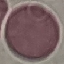
{
  "result": "negative for malaria parasites",
  "capture": "smartphone camera at the microscope eyepiece",
  "stain": "Giemsa",
  "image_type": "cell patch, automatically extracted from a larger field of view and resized to 64 × 64 pixels",
  "preparation": "thin blood smear"
}